Outline each blood parasite and name the species.
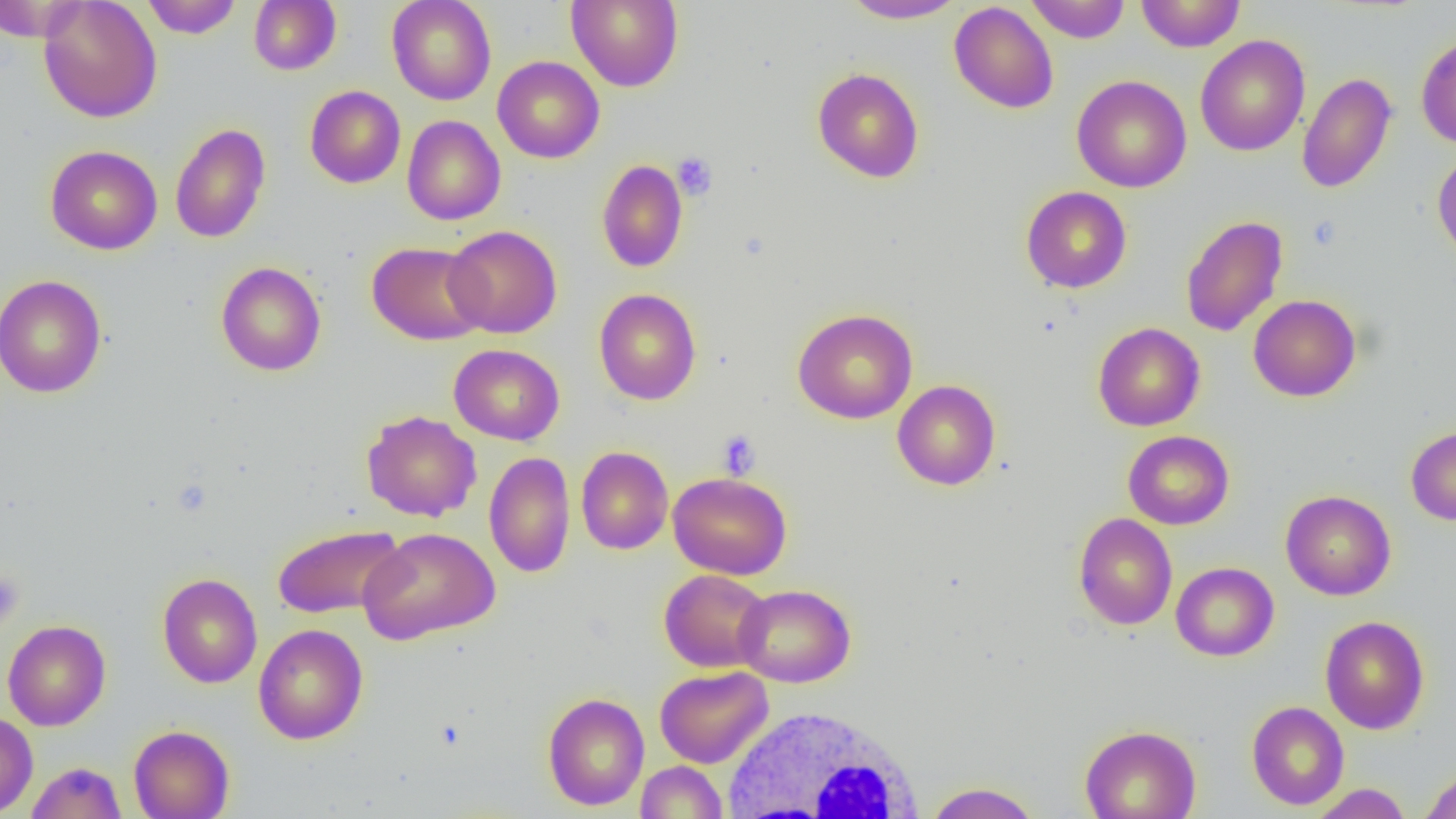
No blood parasites observed.

Summary:
  - Coordinate format: approximate bounding boxes as named x1/y1/x2/y2 corners in pixels
  - White blood cell locations: (x1=655, y1=668, x2=774, y2=772), (x1=721, y1=704, x2=926, y2=818)
  - Platelet locations: (x1=672, y1=152, x2=718, y2=200), (x1=717, y1=430, x2=760, y2=479), (x1=0, y1=568, x2=24, y2=632)
  - Uninfected red blood cell locations: (x1=0, y1=0, x2=86, y2=42), (x1=38, y1=0, x2=162, y2=123), (x1=141, y1=0, x2=243, y2=38), (x1=387, y1=0, x2=497, y2=105), (x1=566, y1=0, x2=684, y2=91), (x1=840, y1=0, x2=967, y2=24), (x1=1026, y1=0, x2=1130, y2=43), (x1=1136, y1=0, x2=1246, y2=52), (x1=249, y1=1, x2=341, y2=75), (x1=949, y1=2, x2=1059, y2=114), (x1=1195, y1=34, x2=1310, y2=157), (x1=1416, y1=34, x2=1456, y2=148), (x1=493, y1=56, x2=605, y2=163), (x1=812, y1=67, x2=924, y2=183), (x1=1297, y1=72, x2=1397, y2=193), (x1=1071, y1=75, x2=1192, y2=193), (x1=305, y1=85, x2=406, y2=188), (x1=402, y1=115, x2=505, y2=225), (x1=170, y1=123, x2=271, y2=243), (x1=45, y1=145, x2=163, y2=254), (x1=1432, y1=149, x2=1456, y2=262), (x1=596, y1=159, x2=687, y2=273), (x1=1021, y1=186, x2=1132, y2=293), (x1=1180, y1=214, x2=1288, y2=337), (x1=444, y1=225, x2=562, y2=338), (x1=367, y1=241, x2=488, y2=345), (x1=216, y1=261, x2=326, y2=376), (x1=0, y1=274, x2=107, y2=398), (x1=594, y1=288, x2=702, y2=405), (x1=1248, y1=294, x2=1361, y2=401), (x1=792, y1=308, x2=918, y2=424), (x1=1093, y1=322, x2=1205, y2=431), (x1=449, y1=344, x2=564, y2=445), (x1=892, y1=380, x2=1001, y2=490), (x1=361, y1=410, x2=482, y2=522), (x1=1406, y1=425, x2=1456, y2=525), (x1=1123, y1=430, x2=1234, y2=529), (x1=576, y1=447, x2=673, y2=555), (x1=484, y1=451, x2=576, y2=578), (x1=668, y1=471, x2=793, y2=580), (x1=1280, y1=490, x2=1396, y2=600), (x1=1073, y1=513, x2=1177, y2=630), (x1=271, y1=524, x2=407, y2=620), (x1=359, y1=527, x2=500, y2=645), (x1=1171, y1=562, x2=1279, y2=661), (x1=660, y1=569, x2=772, y2=672), (x1=157, y1=573, x2=263, y2=688), (x1=734, y1=583, x2=856, y2=687), (x1=1320, y1=615, x2=1430, y2=734), (x1=3, y1=620, x2=111, y2=731), (x1=254, y1=623, x2=368, y2=745), (x1=655, y1=666, x2=772, y2=768), (x1=542, y1=692, x2=650, y2=810), (x1=1246, y1=701, x2=1349, y2=810), (x1=0, y1=711, x2=38, y2=817), (x1=1079, y1=724, x2=1201, y2=819), (x1=128, y1=725, x2=234, y2=819), (x1=636, y1=760, x2=728, y2=818), (x1=26, y1=761, x2=127, y2=818), (x1=1419, y1=768, x2=1456, y2=819), (x1=923, y1=782, x2=1042, y2=819), (x1=1307, y1=783, x2=1413, y2=818)
  - Slide-level diagnosis: negative for blood parasites
  - Preparation: thin blood smear
  - Field of view: single
  - Image size: 1456×819 pixels
  - Modality: optical microscopy
  - Magnification: 1000x